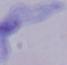 Photomicrograph. A trypanosome is shown. 1000x magnification.